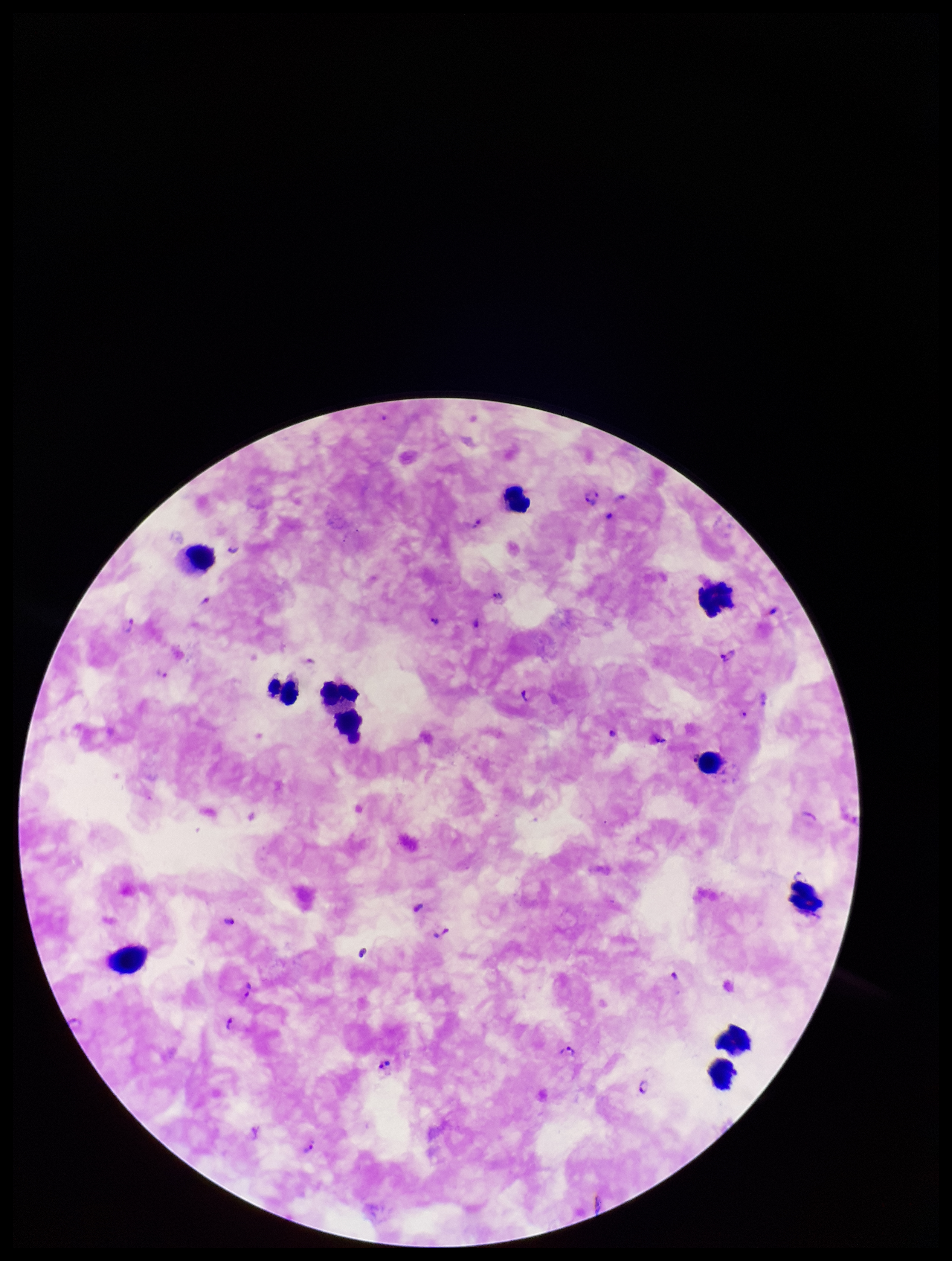

patient malaria status = infected
image size = 952×1261 pixels
species reported for this patient = Plasmodium falciparum
stain = Giemsa
field of view = one from this slide
preparation = thick blood smear
leukocyte count = 11
parasite count = 30
capture = smartphone photograph through the microscope eyepiece
Plasmodium parasites = seen